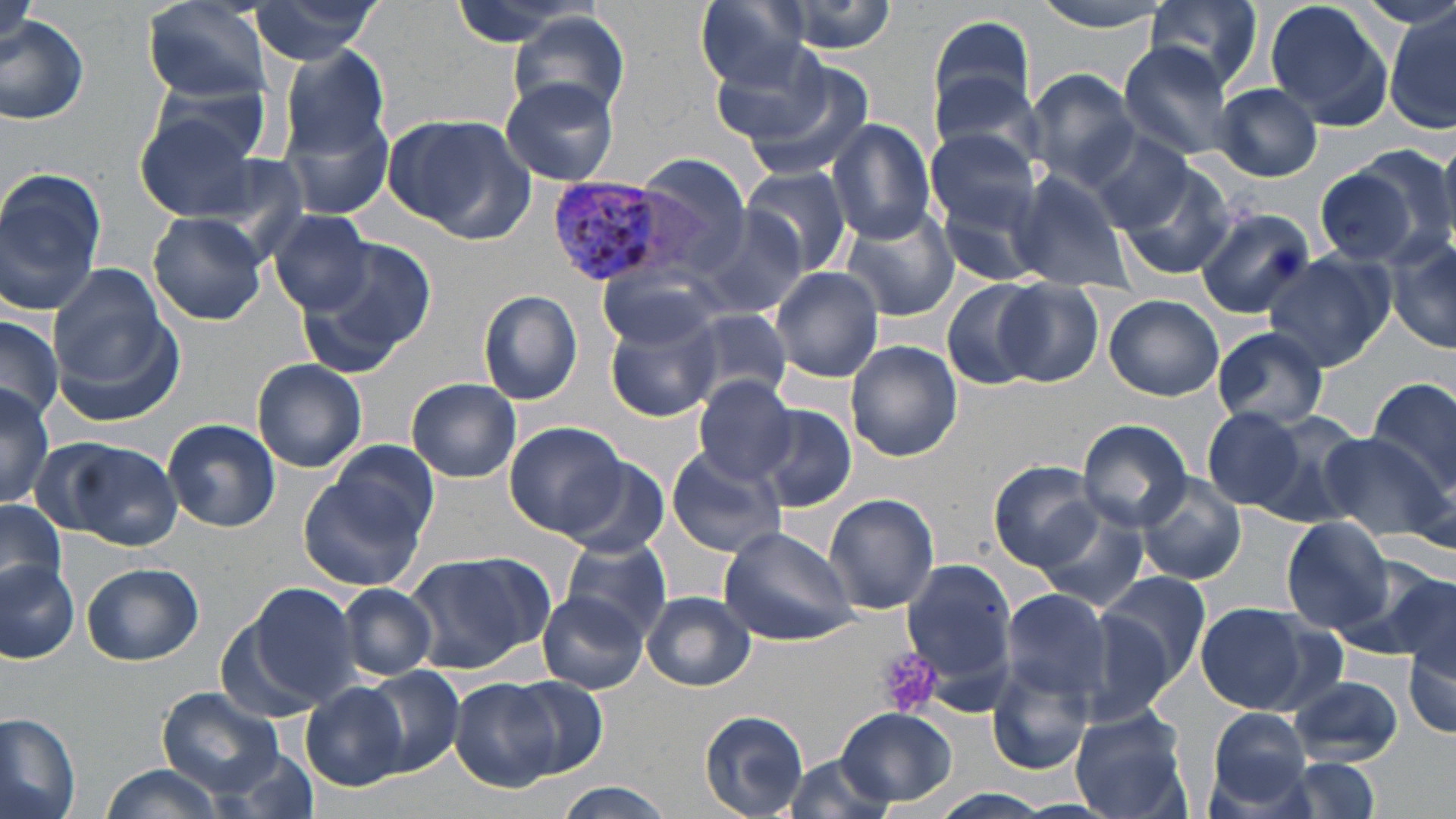
Approximate bounding boxes as named x1/y1/x2/y2 corners in pixels. Platelet locations: (x1=879, y1=648, x2=942, y2=718). Plasmodium vivax-infected red blood cell locations: (x1=548, y1=181, x2=676, y2=286). Uninfected red blood cell locations: (x1=140, y1=0, x2=273, y2=103), (x1=245, y1=0, x2=385, y2=64), (x1=695, y1=0, x2=812, y2=89), (x1=766, y1=0, x2=901, y2=54), (x1=1031, y1=0, x2=1175, y2=36), (x1=1142, y1=0, x2=1267, y2=94), (x1=1267, y1=3, x2=1393, y2=129), (x1=510, y1=10, x2=630, y2=119), (x1=1388, y1=10, x2=1456, y2=134), (x1=1, y1=11, x2=89, y2=127), (x1=929, y1=14, x2=1037, y2=124), (x1=1118, y1=42, x2=1239, y2=161), (x1=712, y1=43, x2=839, y2=150), (x1=278, y1=45, x2=392, y2=159), (x1=741, y1=63, x2=878, y2=183), (x1=1027, y1=70, x2=1140, y2=189), (x1=928, y1=74, x2=1047, y2=172), (x1=151, y1=75, x2=273, y2=167), (x1=499, y1=78, x2=621, y2=187), (x1=1212, y1=83, x2=1322, y2=181), (x1=133, y1=112, x2=267, y2=223), (x1=284, y1=114, x2=394, y2=221), (x1=388, y1=114, x2=532, y2=241), (x1=827, y1=118, x2=938, y2=243), (x1=925, y1=128, x2=1042, y2=235), (x1=1084, y1=130, x2=1197, y2=232), (x1=632, y1=153, x2=756, y2=275), (x1=1114, y1=163, x2=1238, y2=282), (x1=1314, y1=163, x2=1427, y2=267), (x1=741, y1=165, x2=852, y2=276), (x1=0, y1=168, x2=107, y2=312), (x1=1005, y1=168, x2=1134, y2=290), (x1=937, y1=182, x2=1051, y2=286), (x1=1195, y1=207, x2=1316, y2=317), (x1=840, y1=208, x2=959, y2=321), (x1=149, y1=211, x2=267, y2=327), (x1=270, y1=211, x2=373, y2=317), (x1=690, y1=211, x2=810, y2=322), (x1=1386, y1=232, x2=1456, y2=355), (x1=297, y1=235, x2=437, y2=369), (x1=1265, y1=250, x2=1395, y2=370), (x1=46, y1=261, x2=175, y2=391), (x1=770, y1=266, x2=882, y2=383), (x1=600, y1=268, x2=721, y2=351), (x1=942, y1=280, x2=1049, y2=392), (x1=996, y1=280, x2=1104, y2=386), (x1=479, y1=289, x2=583, y2=405), (x1=1104, y1=294, x2=1224, y2=401), (x1=685, y1=308, x2=794, y2=406), (x1=606, y1=311, x2=722, y2=422), (x1=0, y1=315, x2=64, y2=421), (x1=1212, y1=329, x2=1329, y2=428), (x1=845, y1=340, x2=961, y2=462), (x1=251, y1=358, x2=368, y2=473), (x1=692, y1=375, x2=798, y2=484), (x1=1365, y1=375, x2=1456, y2=496), (x1=407, y1=377, x2=522, y2=482), (x1=0, y1=378, x2=55, y2=510), (x1=757, y1=403, x2=858, y2=513), (x1=1202, y1=407, x2=1307, y2=509), (x1=1236, y1=408, x2=1370, y2=525), (x1=162, y1=418, x2=280, y2=532), (x1=1077, y1=418, x2=1191, y2=532), (x1=505, y1=420, x2=627, y2=537), (x1=1314, y1=433, x2=1448, y2=542), (x1=55, y1=438, x2=185, y2=550), (x1=328, y1=441, x2=437, y2=542), (x1=665, y1=446, x2=788, y2=557), (x1=560, y1=460, x2=669, y2=557), (x1=989, y1=460, x2=1103, y2=571), (x1=298, y1=463, x2=431, y2=590), (x1=1135, y1=472, x2=1247, y2=585), (x1=824, y1=494, x2=940, y2=615), (x1=0, y1=499, x2=67, y2=596), (x1=1034, y1=505, x2=1149, y2=611), (x1=1281, y1=517, x2=1392, y2=632), (x1=718, y1=525, x2=861, y2=643), (x1=560, y1=537, x2=673, y2=639), (x1=402, y1=553, x2=545, y2=674), (x1=899, y1=556, x2=1018, y2=687), (x1=1353, y1=558, x2=1455, y2=662), (x1=0, y1=559, x2=80, y2=663), (x1=81, y1=562, x2=204, y2=666), (x1=1098, y1=571, x2=1211, y2=687), (x1=1396, y1=574, x2=1454, y2=680), (x1=243, y1=582, x2=364, y2=708), (x1=336, y1=584, x2=438, y2=680), (x1=999, y1=588, x2=1114, y2=704), (x1=539, y1=591, x2=649, y2=693), (x1=641, y1=591, x2=754, y2=690), (x1=1194, y1=602, x2=1322, y2=714), (x1=1073, y1=614, x2=1177, y2=726), (x1=1404, y1=641, x2=1456, y2=740), (x1=987, y1=659, x2=1096, y2=775), (x1=363, y1=666, x2=464, y2=776), (x1=1288, y1=674, x2=1406, y2=764), (x1=505, y1=676, x2=609, y2=780), (x1=450, y1=679, x2=557, y2=790), (x1=301, y1=682, x2=406, y2=790), (x1=157, y1=685, x2=290, y2=798), (x1=1068, y1=705, x2=1193, y2=818), (x1=837, y1=709, x2=957, y2=804), (x1=699, y1=710, x2=810, y2=816), (x1=1203, y1=710, x2=1316, y2=814), (x1=0, y1=712, x2=81, y2=819), (x1=215, y1=748, x2=320, y2=819), (x1=778, y1=755, x2=902, y2=818), (x1=1262, y1=757, x2=1388, y2=819), (x1=98, y1=765, x2=227, y2=819), (x1=550, y1=785, x2=675, y2=818), (x1=924, y1=791, x2=1070, y2=819). Slide-level diagnosis: Plasmodium vivax. Image is 1456×819 pixels. Light microscopy. Captured at 1000x magnification. One field of a larger specimen. Thin blood film. May-Grünwald-Giemsa-stained preparation.